Classify this cell by malaria status.
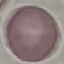
It is uninfected.

Automatically extracted cell patch, resized to 64 × 64 pixels. Thin blood film. Giemsa stain. Acquired by smartphone through the microscope eyepiece.